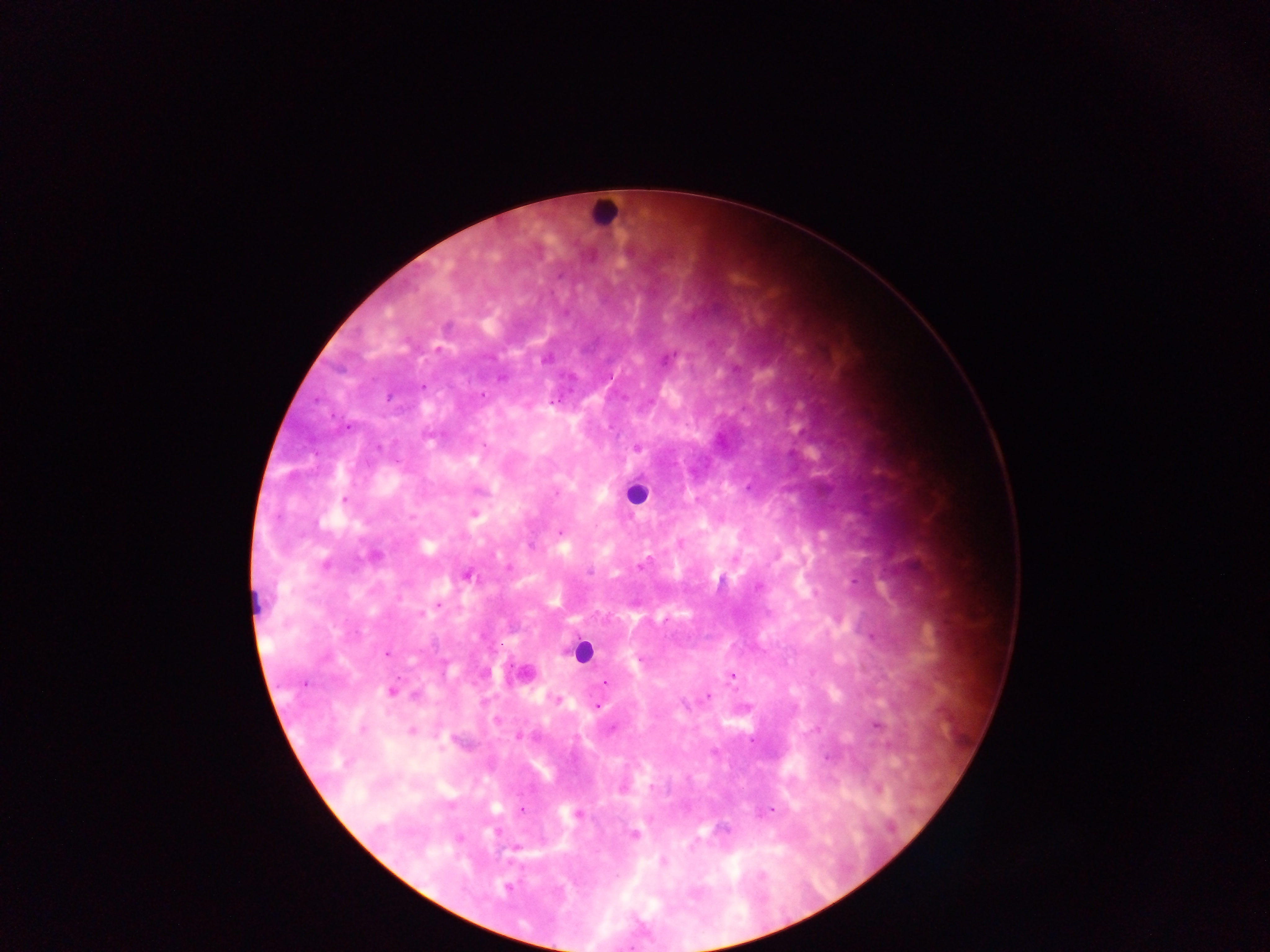
Approximate centers as {x, y} in pixels. Leukocyte locations: {603, 214}, {636, 494}, {581, 651}, {526, 672}. Malaria parasite locations: {558, 276}, {546, 360}, {501, 378}, {422, 387}, {483, 395}, {388, 397}, {316, 401}, {552, 401}, {347, 428}, {637, 447}, {396, 461}, {556, 493}, {344, 499}, {473, 513}, {412, 517}, {559, 532}, {326, 565}, {641, 566}, {590, 572}, {467, 576}, {759, 587}, {440, 605}, {422, 613}, {387, 653}, {641, 659}, {731, 677}, {605, 683}, {304, 684}, {391, 690}, {708, 696}, {557, 700}, {597, 707}, {877, 726}, {363, 730}, {412, 730}, {751, 741}, {827, 758}, {652, 787}, {878, 790}, {522, 810}, {772, 810}, {577, 815}, {891, 828}, {633, 834}, {662, 862}, {506, 887}. Thick blood film. Photographed through a microscope with a mobile-phone camera. One field of view. Collected in Ghana. Image is 1270×952 pixels.